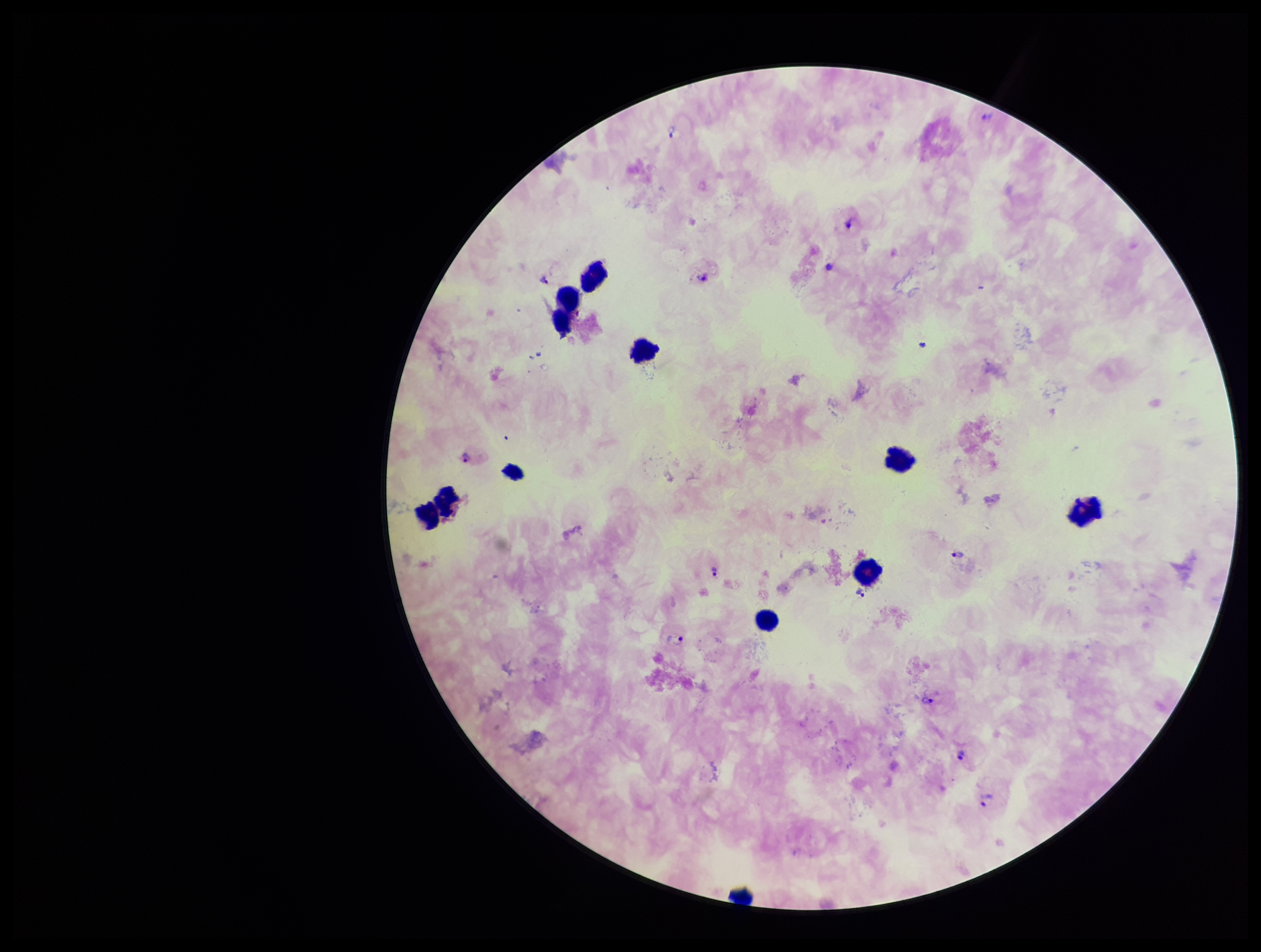
Species reported for this patient: Plasmodium vivax. Patient malaria status: infected. Giemsa stain. Plasmodium parasites: detected. Leukocyte count: 11. Parasite count: 11. Preparation: thick smear. Smartphone photograph taken through the eyepiece of a microscope. One field from this slide. Image is 1261×952 pixels.